State which parasite is depicted.
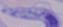

This is a trypanosome.

Captured at 1000x magnification. Photomicrograph.